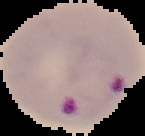

Result: Plasmodium parasites identified. The area outside the segmented cell region is set to black. From a thin blood smear. Image is 145×136 pixels.